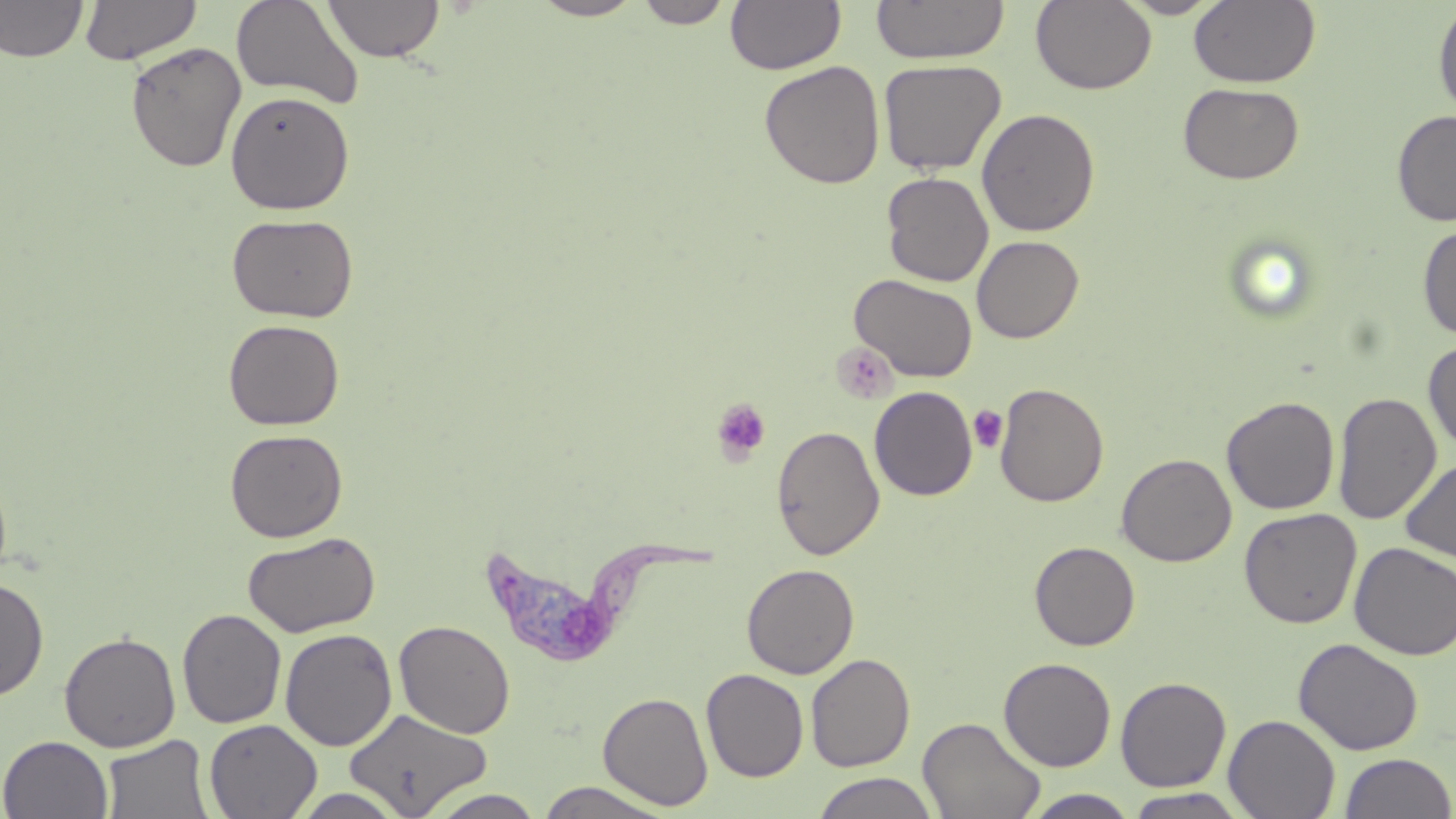

slide-level diagnosis = Trypanosoma brucei
stain = May-Grünwald-Giemsa
preparation = thin blood smear
magnification = 1000x
platelet locations = approximate bounding boxes as (x1,y1)-(x2,y2) corner pairs in pixels: (836,344)-(901,403), (711,397)-(772,463), (967,405)-(1008,453)
modality = light microscopy
field of view = one of a larger specimen
uninfected red blood cell locations = approximate bounding boxes as (x1,y1)-(x2,y2) corner pairs in pixels: (0,0)-(88,62), (80,0)-(201,65), (231,0)-(365,111), (324,0)-(444,62), (530,0)-(645,21), (635,0)-(733,28), (725,0)-(846,75), (872,0)-(1010,64), (1031,0)-(1156,94), (1119,0)-(1225,18), (1189,0)-(1321,88), (1432,2)-(1456,119), (125,41)-(246,172), (878,59)-(1006,175), (759,61)-(885,189), (1178,82)-(1305,184), (225,91)-(354,215), (976,108)-(1100,237), (1392,110)-(1456,227), (881,172)-(994,286), (226,212)-(359,323), (1417,224)-(1456,341), (971,235)-(1084,343), (850,273)-(978,382), (223,319)-(344,430), (1423,338)-(1456,454), (995,382)-(1109,507), (869,386)-(978,501), (1333,392)-(1441,524), (1221,395)-(1340,515), (771,425)-(885,560), (225,428)-(348,542), (1116,453)-(1236,566), (1400,457)-(1456,565), (1238,507)-(1362,628), (242,531)-(380,638), (1030,541)-(1140,650), (1350,542)-(1456,660), (741,563)-(859,679), (0,575)-(49,701), (177,608)-(286,729), (394,619)-(516,739), (280,628)-(397,751), (59,632)-(180,751), (1293,637)-(1423,755), (805,653)-(915,772), (999,657)-(1116,771), (701,668)-(808,782), (998,670)-(1231,780), (1115,676)-(1232,792), (598,691)-(713,810), (343,708)-(493,816), (1223,714)-(1340,819), (918,716)-(1046,819), (203,718)-(323,819), (101,734)-(214,818), (0,735)-(114,819), (1338,752)-(1455,818), (812,772)-(939,819), (534,782)-(676,818), (288,787)-(411,818), (1123,788)-(1252,818), (424,789)-(548,818), (1023,789)-(1139,818)
Trypanosoma brucei locations = approximate bounding boxes as (x1,y1)-(x2,y2) corner pairs in pixels: (487,537)-(728,668)
image size = 1456×819 pixels